Report the malaria status of this cell.
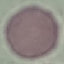
It is uninfected.

Summary:
  - Image type: automatically extracted cell patch, resized to 64 × 64 pixels
  - Stain: Giemsa
  - Preparation: thin blood film
  - Capture: smartphone through the microscope eyepiece